State which cell type is depicted.
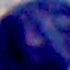
This is a leukocyte.

modality = photomicrograph
magnification = 1000x